Mark where platelets are.
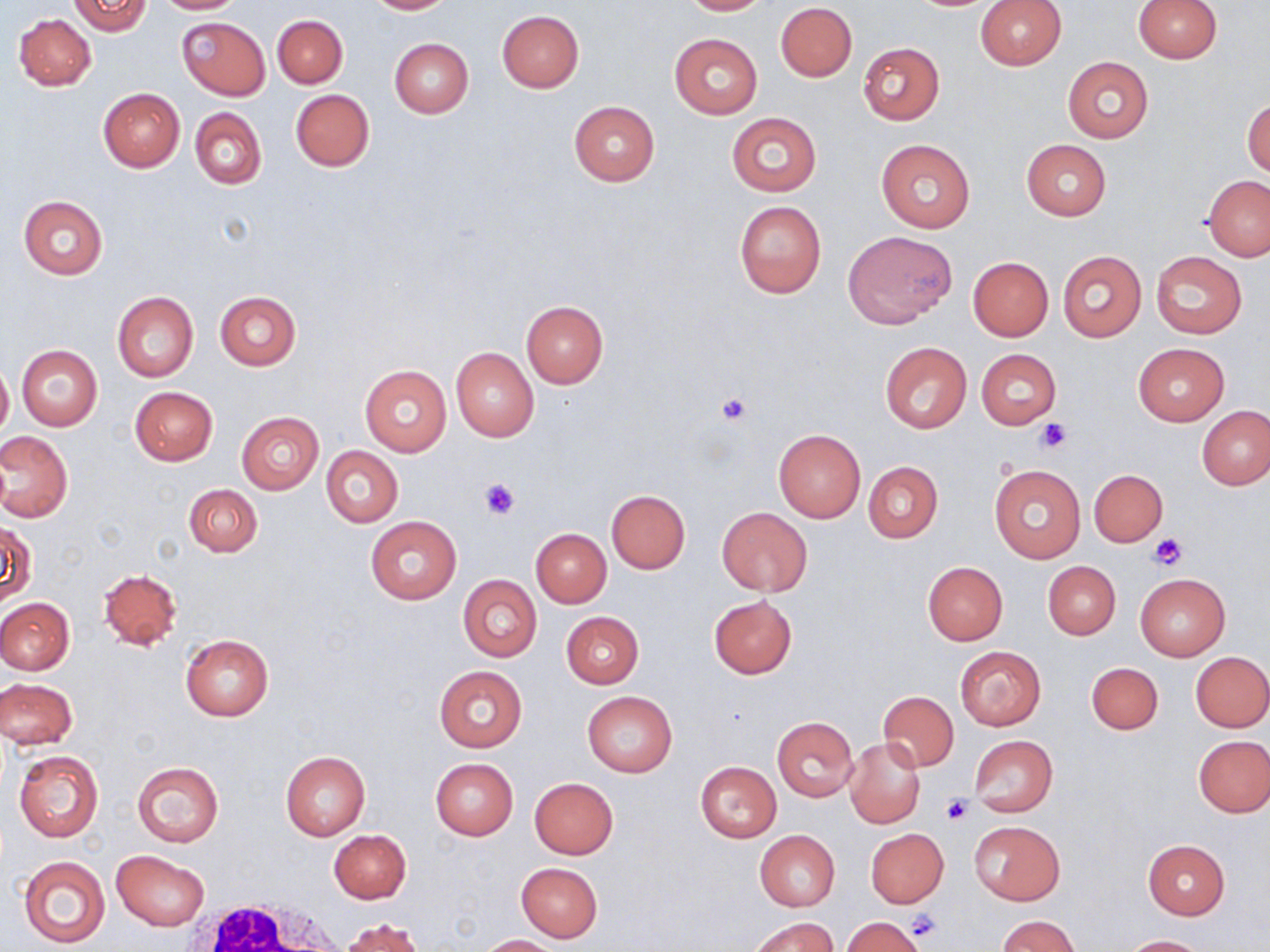

Approximate bounding boxes as (x1, y1, x2, y2) in pixels.
Platelets: (717, 392, 751, 425), (1034, 417, 1071, 453), (479, 478, 520, 520), (1150, 534, 1188, 569), (940, 795, 973, 827), (905, 909, 944, 943).

Uninfected red blood cell locations: (71, 0, 151, 36), (153, 0, 244, 14), (362, 0, 455, 14), (678, 0, 772, 15), (1132, 0, 1222, 62), (976, 1, 1066, 71), (775, 3, 857, 81), (497, 11, 584, 93), (14, 13, 96, 90), (273, 15, 348, 88), (176, 17, 271, 100), (670, 33, 762, 118), (389, 38, 474, 117), (858, 42, 945, 125), (1062, 57, 1153, 142), (98, 87, 184, 172), (290, 89, 374, 170), (1242, 96, 1270, 178), (569, 101, 660, 186), (191, 108, 266, 189), (726, 113, 822, 196), (876, 138, 976, 232), (1021, 140, 1110, 220), (1203, 175, 1270, 261), (19, 195, 108, 279), (734, 200, 826, 298), (843, 231, 956, 327), (1057, 250, 1147, 343), (1150, 250, 1248, 339), (968, 257, 1053, 341), (214, 290, 301, 370), (112, 292, 199, 382), (520, 300, 609, 388), (878, 340, 972, 434), (1132, 343, 1229, 425), (17, 345, 102, 431), (451, 347, 539, 441), (976, 349, 1060, 429), (0, 363, 13, 438), (360, 364, 452, 456), (130, 386, 218, 466), (1198, 406, 1269, 490), (237, 411, 324, 494), (773, 429, 866, 523), (0, 431, 72, 522), (321, 445, 403, 527), (863, 461, 942, 543), (988, 463, 1086, 564), (1089, 469, 1168, 546), (184, 484, 261, 557), (605, 490, 690, 574), (718, 507, 812, 596), (365, 516, 460, 603), (3, 521, 35, 605), (530, 529, 611, 607), (923, 561, 1008, 644), (1044, 561, 1120, 639), (98, 568, 182, 651), (458, 574, 541, 662), (1134, 574, 1231, 661), (708, 595, 798, 678), (0, 598, 74, 675), (562, 612, 644, 688), (180, 633, 274, 721), (954, 646, 1046, 731), (1190, 651, 1270, 732), (1086, 661, 1163, 734), (433, 664, 527, 752), (0, 677, 77, 749), (583, 690, 678, 778), (878, 691, 958, 772), (772, 718, 859, 801), (969, 735, 1057, 816), (1194, 735, 1270, 817), (845, 738, 926, 828), (13, 750, 104, 843), (280, 751, 369, 840), (431, 758, 518, 840), (132, 762, 224, 847), (695, 762, 781, 842), (529, 777, 619, 859), (970, 820, 1064, 906), (328, 829, 411, 903), (866, 829, 949, 907), (754, 830, 840, 911), (1143, 839, 1230, 919), (111, 850, 209, 930), (18, 855, 110, 947), (516, 862, 603, 941), (750, 915, 838, 952), (999, 916, 1078, 952), (845, 917, 924, 951), (339, 918, 425, 952), (479, 934, 558, 951), (1122, 935, 1210, 952). White blood cell locations: (179, 896, 349, 952). Slide-level diagnosis: negative for blood parasites. Captured at 1000x magnification. Optical microscopy. Image is 1270×952 pixels. Thin blood film. May-Grünwald-Giemsa-stained preparation. One field of a larger specimen.